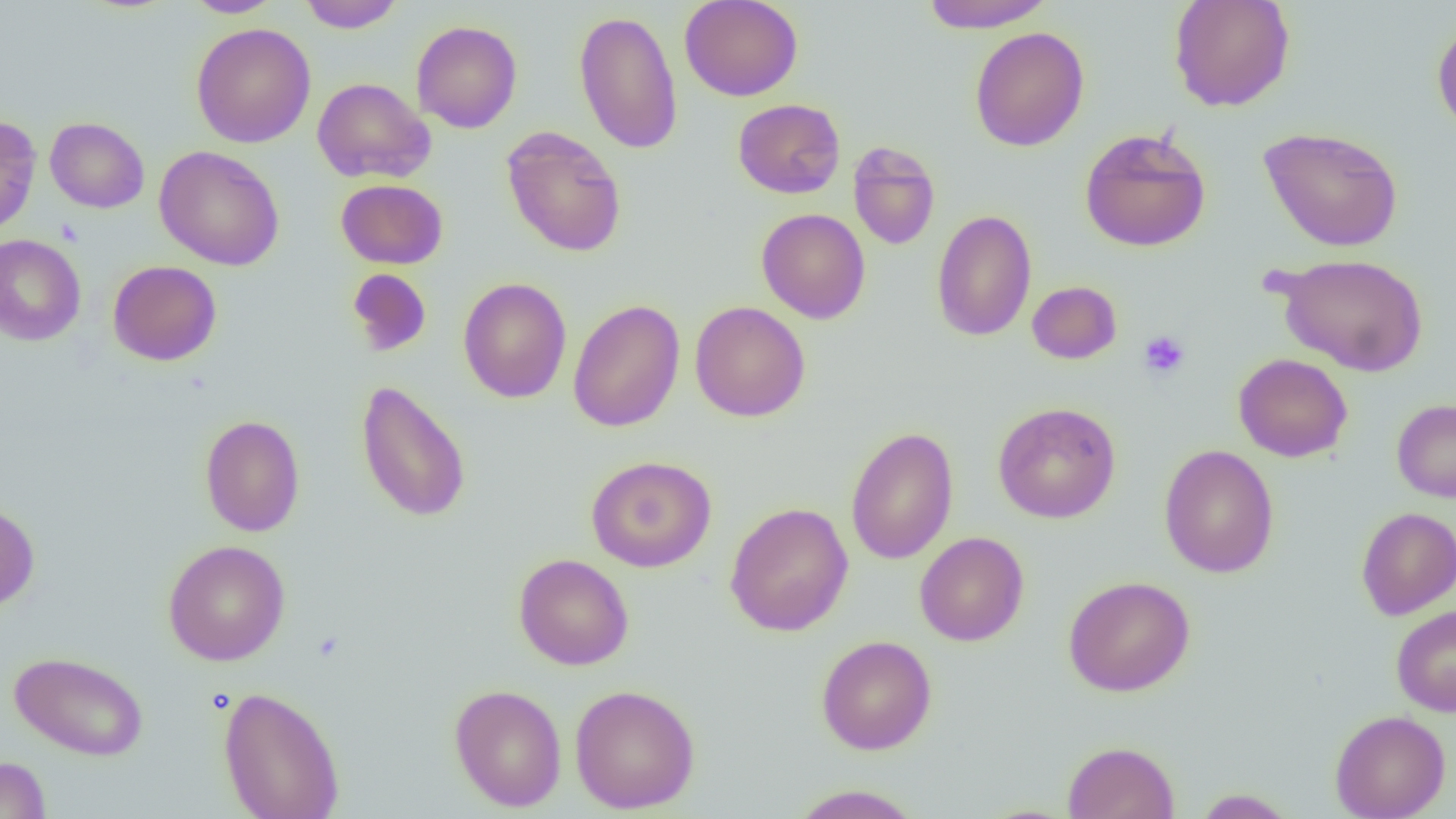

Summary:
  - Coordinate format: approximate bounding boxes as (x1,y1)-(x2,y2) corner pairs in pixels
  - Platelet locations: (1139,331)-(1190,379)
  - Uninfected red blood cell locations: (182,0)-(285,17), (299,0)-(405,32), (679,0)-(803,101), (918,0)-(1054,31), (1168,0)-(1296,112), (573,9)-(683,155), (1432,18)-(1456,139), (411,20)-(522,134), (192,22)-(316,148), (969,26)-(1089,152), (312,77)-(435,184), (733,98)-(846,198), (0,115)-(41,235), (45,117)-(150,213), (500,125)-(628,257), (1259,126)-(1404,252), (1079,128)-(1211,252), (848,141)-(941,250), (154,145)-(285,271), (336,179)-(448,269), (756,208)-(871,324), (931,209)-(1037,341), (0,234)-(86,347), (1273,253)-(1430,376), (108,260)-(222,366), (347,268)-(432,357), (458,277)-(572,403), (1027,280)-(1122,364), (568,299)-(685,432), (689,301)-(810,422), (1233,353)-(1353,462), (355,379)-(472,523), (1391,399)-(1456,502), (993,402)-(1121,524), (200,414)-(305,536), (845,426)-(958,565), (1159,444)-(1279,578), (586,455)-(717,572), (0,502)-(40,612), (725,502)-(853,636), (1356,507)-(1456,620), (915,532)-(1029,647), (162,539)-(291,665), (514,553)-(633,670), (1063,575)-(1195,697), (1391,605)-(1456,717), (816,635)-(937,755), (9,651)-(148,761), (449,683)-(567,812), (570,684)-(701,814), (219,686)-(344,819), (1330,710)-(1451,819), (1062,741)-(1180,819), (0,756)-(50,819), (788,784)-(924,818), (1193,788)-(1298,818)
  - Slide-level diagnosis: no evidence of blood parasites
  - Modality: optical microscopy
  - Magnification: 1000x
  - Image size: 1456×819 pixels
  - Preparation: thin blood film
  - Field of view: single